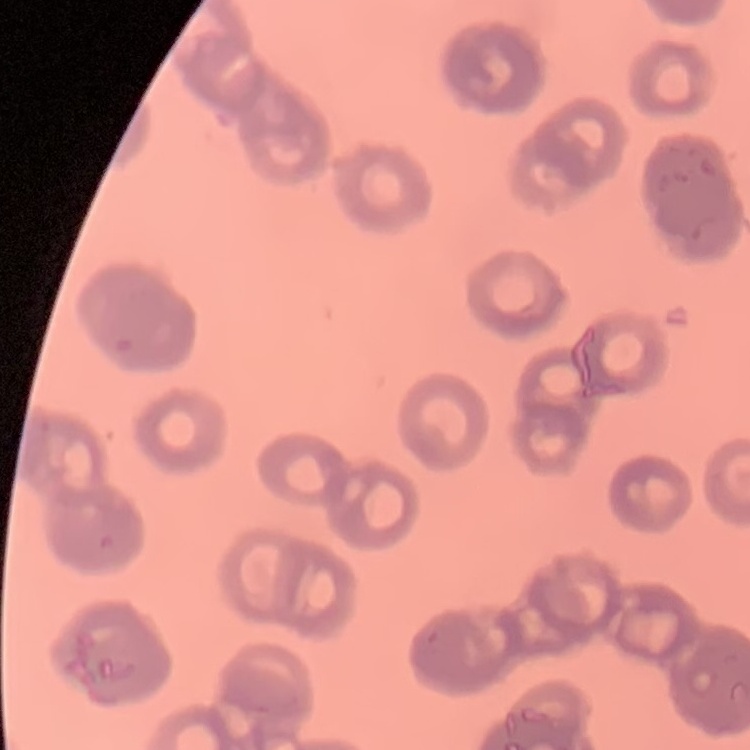
red blood cell morphology = rouleaux formation
image type = one tile cut from a larger photomicrograph
preparation = thin blood smear
stain = Field's or Giemsa